Classify this cell by malaria status.
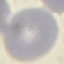

Uninfected.

image_type: automatically extracted cell patch, resized to 64 × 64 pixels
capture: smartphone through the microscope eyepiece
preparation: thin blood film
stain: Giemsa